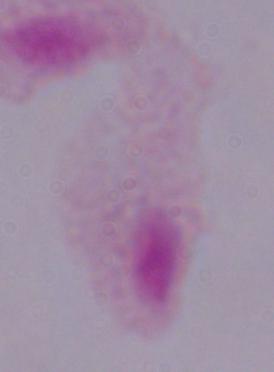
identification: trichomonad
modality: micrograph
magnification: 1000x